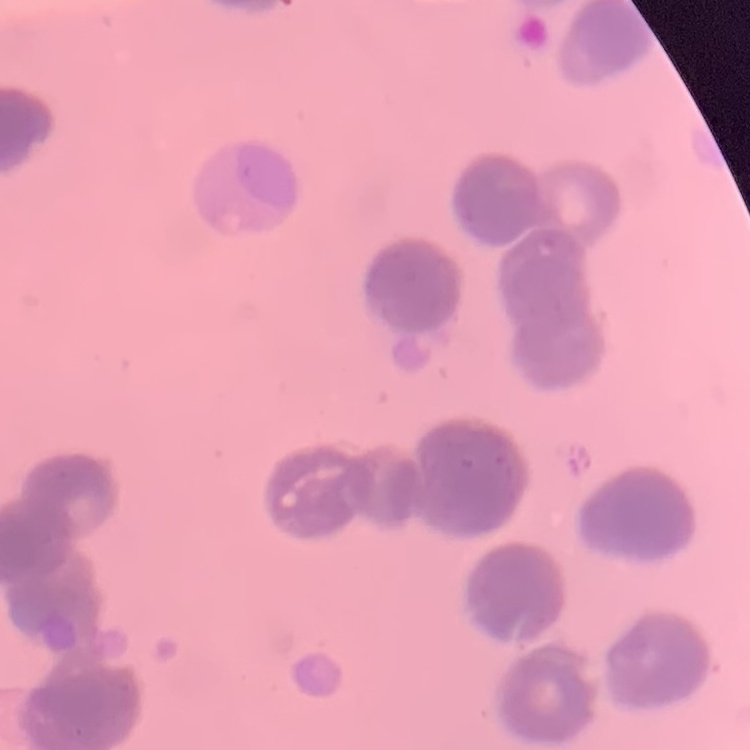
red blood cell morphology = rouleaux formation
stain = Field's or Giemsa
preparation = thin blood smear
image type = square crop of a larger photomicrograph